Locate every Plasmodium vivax-infected red blood cell.
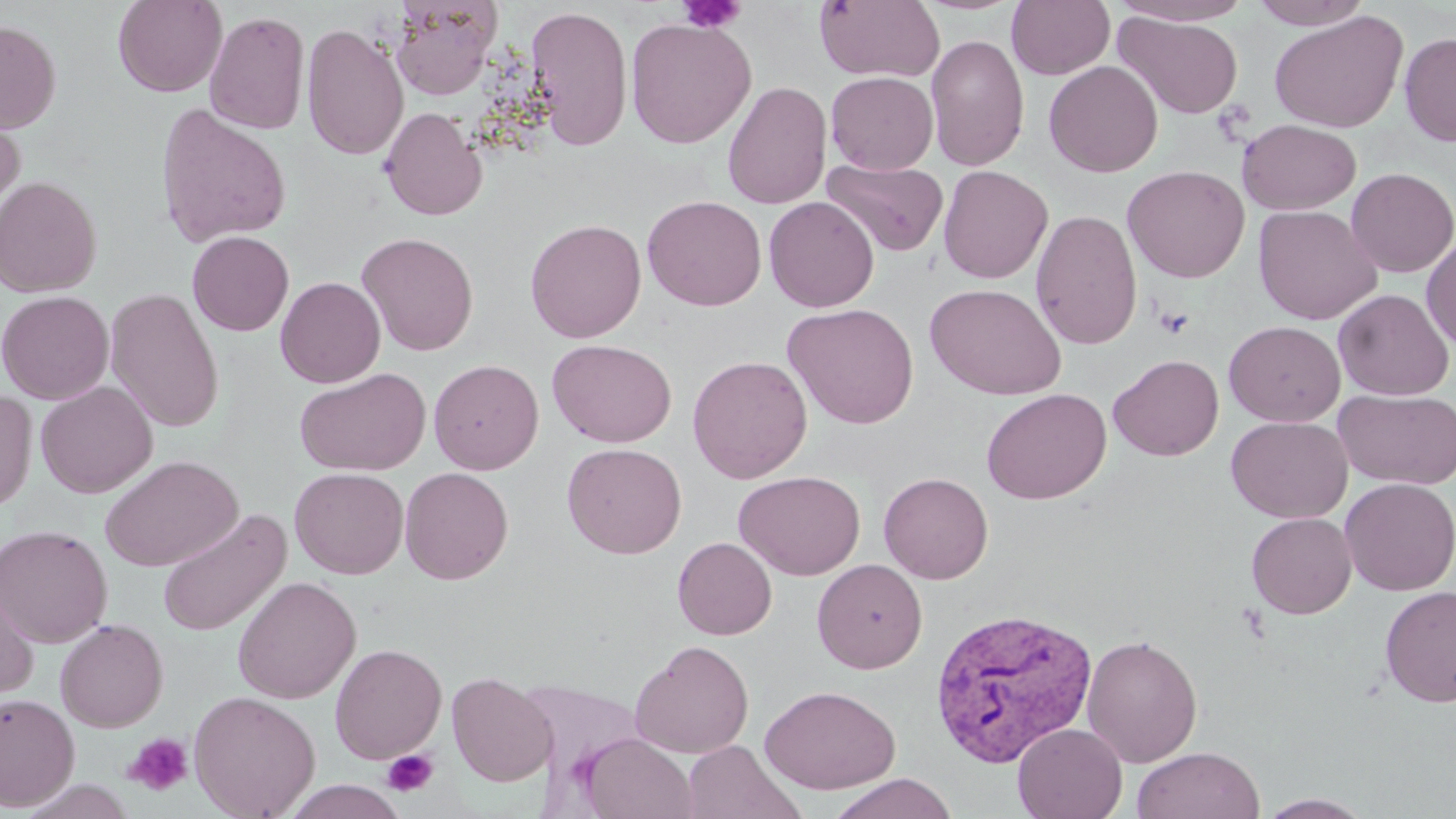

Approximate bounding boxes as (x1,y1)-(x2,y2) corner pairs in pixels.
Plasmodium vivax-infected red blood cells: (930,605)-(1098,766).

slide_level_diagnosis: Plasmodium vivax
field_of_view: one of a larger specimen
image_size: 1456×819 pixels
stain: May-Grünwald-Giemsa
uninfected_red_blood_cell_locations: 'approximate bounding boxes as (x1,y1)-(x2,y2) corner pairs in pixels: (112,0)-(227,97), (815,0)-(945,83), (1006,0)-(1115,80), (1111,0)-(1255,25), (1249,0)-(1373,29), (389,1)-(500,100), (525,5)-(633,151), (204,10)-(311,134), (1269,10)-(1408,133), (1113,11)-(1244,120), (625,17)-(756,148), (0,21)-(61,133), (301,22)-(409,161), (1398,32)-(1456,146), (925,34)-(1029,172), (1044,60)-(1163,177), (825,71)-(939,174), (722,80)-(831,209), (0,102)-(26,226), (154,103)-(292,248), (379,106)-(487,220), (1237,119)-(1361,215), (822,158)-(949,257), (1122,164)-(1250,283), (937,165)-(1053,284), (1346,167)-(1456,278), (0,176)-(102,298), (642,194)-(767,310), (764,196)-(879,313), (1253,205)-(1382,325), (1030,209)-(1143,350), (525,218)-(647,343), (187,230)-(294,336), (356,231)-(479,356), (1421,235)-(1456,352), (275,276)-(386,388), (924,284)-(1067,399), (105,287)-(224,433), (1333,289)-(1454,400), (0,290)-(114,404), (782,302)-(920,429), (1224,320)-(1345,426), (547,339)-(677,447), (1109,354)-(1224,461), (687,355)-(813,483), (429,359)-(543,474), (294,368)-(430,476), (35,381)-(157,498), (0,387)-(37,513), (981,387)-(1111,504), (1334,388)-(1456,490), (1226,416)-(1352,523), (562,442)-(687,558), (100,455)-(243,571), (400,466)-(514,584), (289,467)-(409,579), (733,470)-(866,580), (878,472)-(993,584), (1340,477)-(1456,596), (157,509)-(291,638), (1246,512)-(1357,618), (0,524)-(113,647), (672,537)-(777,639), (812,558)-(928,673), (232,576)-(361,705), (0,577)-(39,702), (1380,586)-(1456,707), (55,618)-(168,732), (1081,633)-(1203,767), (630,640)-(755,758), (330,644)-(447,764), (447,671)-(557,787), (515,678)-(644,781), (760,684)-(901,794), (188,690)-(320,819), (0,692)-(80,811), (1012,723)-(1127,819), (576,732)-(698,819), (681,740)-(799,819), (1131,746)-(1265,819), (827,773)-(958,819), (280,780)-(410,819), (1257,793)-(1374,818)'
modality: light microscopy
magnification: 1000x
platelet_locations: 'approximate bounding boxes as (x1,y1)-(x2,y2) corner pairs in pixels: (678,0)-(745,33), (1153,305)-(1195,339), (123,732)-(194,796), (381,749)-(438,797)'
preparation: thin blood film